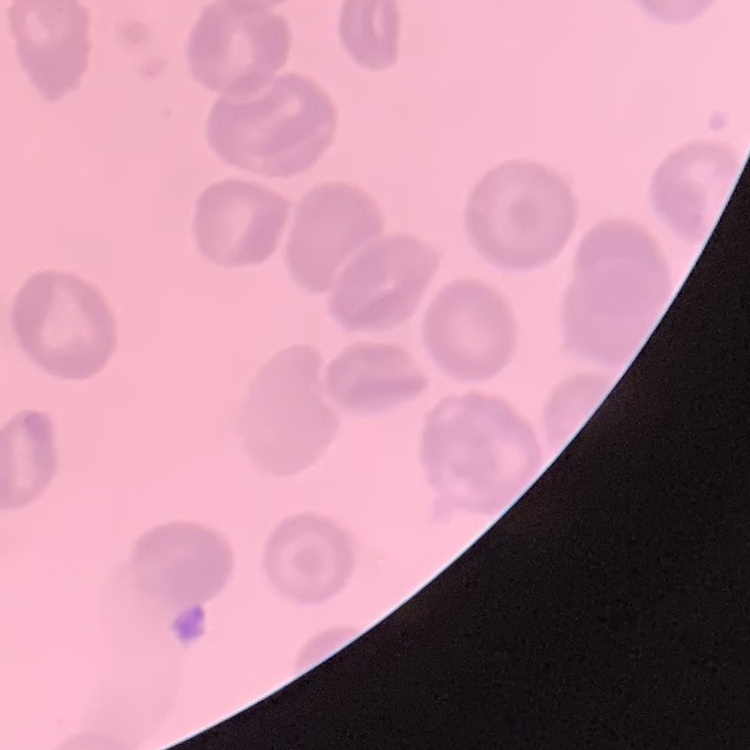

Summary:
  - Erythrocyte morphology: no rouleaux formation
  - Preparation: thin blood film
  - Image type: square crop of a larger photomicrograph
  - Stain: Field's or Giemsa